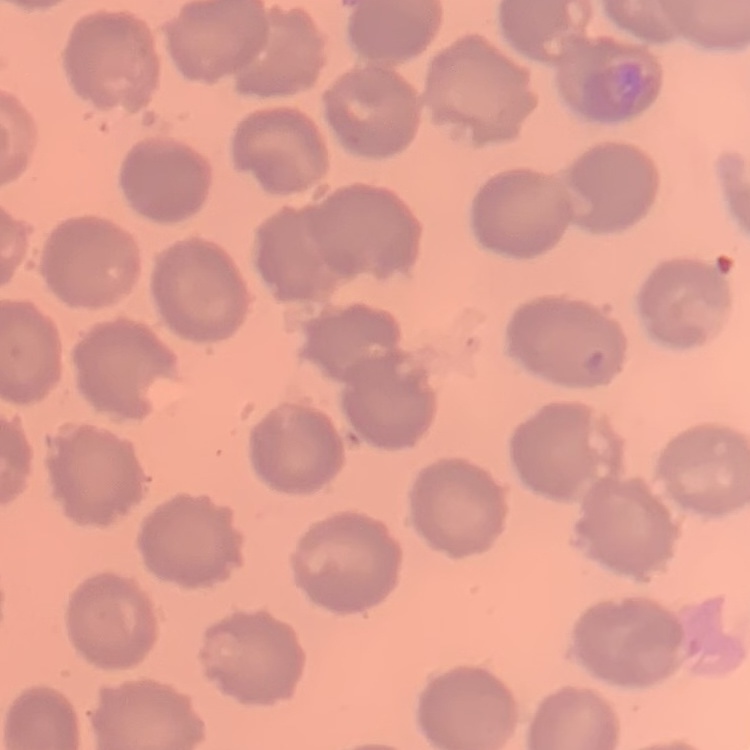 The red blood cells exhibit no rouleaux formation. Field's or Giemsa stain. Thin blood smear. One tile cut from a larger photomicrograph.